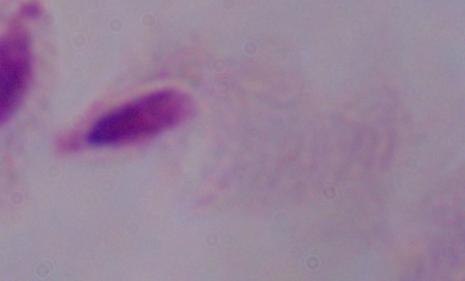

1000x magnification. Micrograph. A trichomonad is shown.